Outline every Plasmodium parasite, every leukocyte, and every artifact (stain precipitate or debris).
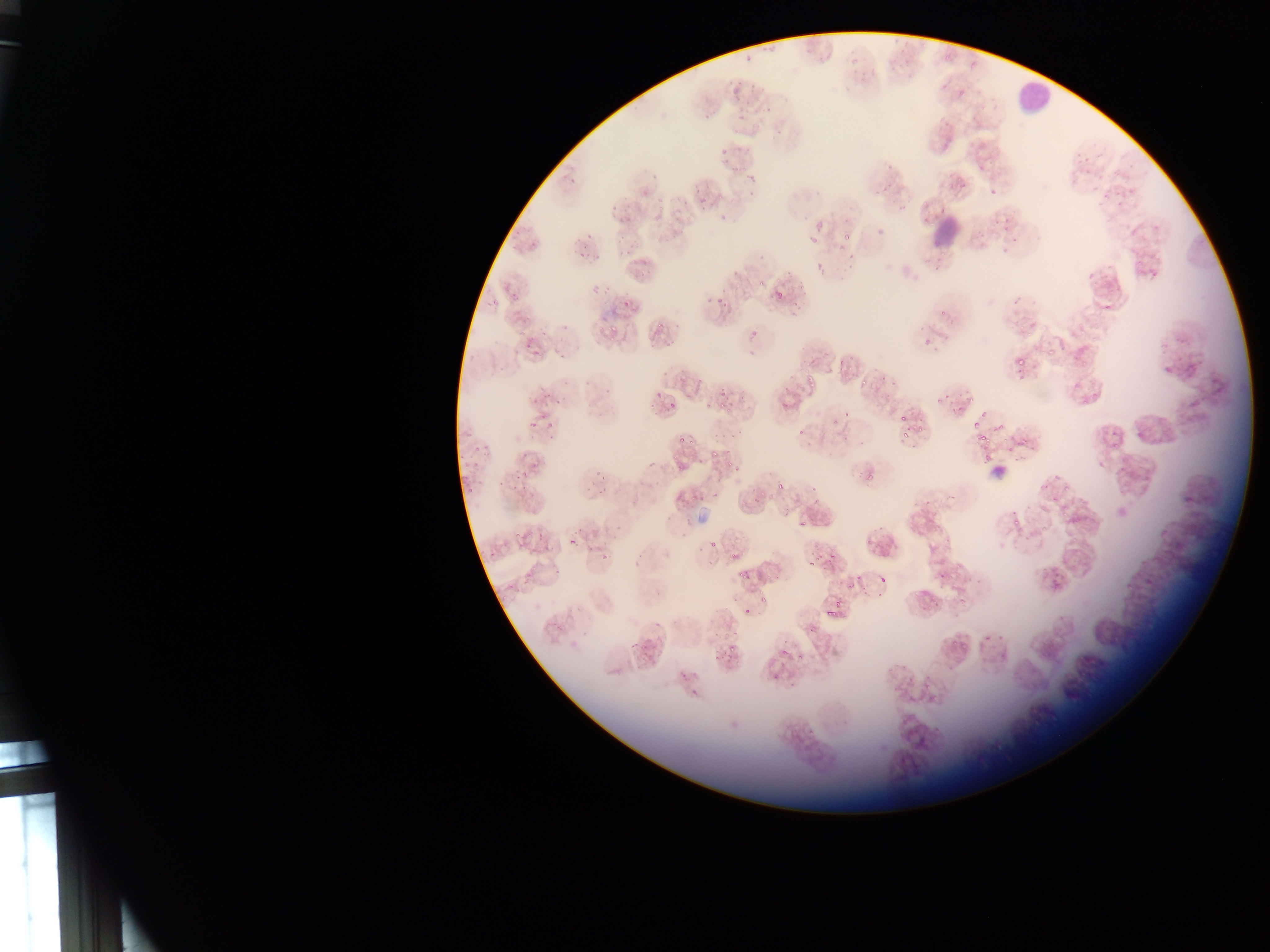

Approximate bounding boxes as left top right bottom in pixels.
Plasmodium parasites: 724 67 759 94; 756 105 779 130; 709 135 741 165; 747 166 761 181; 989 188 997 195; 990 189 1000 198; 694 192 714 211; 607 194 626 210; 719 199 736 224; 619 210 635 221; 815 221 827 232; 842 230 852 240; 616 233 628 243; 583 235 590 245; 809 239 820 244; 837 242 848 252; 624 244 641 256; 593 250 604 264; 577 251 587 259; 816 264 824 274; 634 265 643 276; 756 278 765 286; 596 285 606 291; 720 286 734 303; 774 288 785 296; 506 290 524 306; 788 293 804 314; 657 321 668 329; 608 322 625 339; 516 329 527 338; 751 329 762 336; 524 336 536 351; 1046 348 1054 356; 1011 350 1030 365; 835 356 846 368; 858 367 876 390; 809 368 825 388; 688 372 699 387; 535 385 553 401; 655 387 665 399; 716 392 731 406; 947 394 970 411; 704 396 713 410; 552 398 560 404; 665 398 676 415; 841 411 851 421; 897 412 908 423; 971 414 1000 446; 524 415 540 430; 545 415 559 429; 917 422 929 433; 796 425 807 440; 1109 427 1119 437; 900 433 913 439; 673 435 693 451; 520 440 541 459; 469 442 484 456; 1006 442 1017 454; 1021 442 1038 452; 706 443 719 463; 1110 443 1119 450; 470 455 483 472; 984 455 997 468; 730 462 741 474; 677 466 686 475; 862 467 878 483; 514 471 524 479; 592 474 602 480; 1045 475 1061 491; 775 480 785 490; 1062 484 1073 496; 463 486 474 495; 685 491 704 502; 799 503 823 527; 783 509 791 516; 1012 518 1021 527; 522 521 531 534; 537 524 550 540; 1039 526 1049 533; 1070 532 1081 541; 570 534 582 544; 706 539 720 553; 805 546 822 567; 729 550 739 565; 953 562 962 572; 734 568 749 583; 939 568 947 578; 876 572 889 586; 526 573 537 585; 1048 578 1068 591; 843 582 855 590; 756 584 770 607; 930 596 941 607; 959 596 969 604; 824 610 841 623; 626 629 651 650; 984 632 992 642; 951 640 960 648; 718 643 734 663; 781 648 789 660; 799 652 805 662 | approximate x y pixel centers of objects too small to bound: 626 304; 838 604.
Leukocytes: 1007 81 1043 122; 913 220 969 260.

Summary:
  - Capture: mobile-phone photograph through a microscope
  - Field of view: single
  - Preparation: thin blood smear
  - Image size: 1270×952 pixels
  - Country: Ghana